Describe the morphology of the erythrocytes.
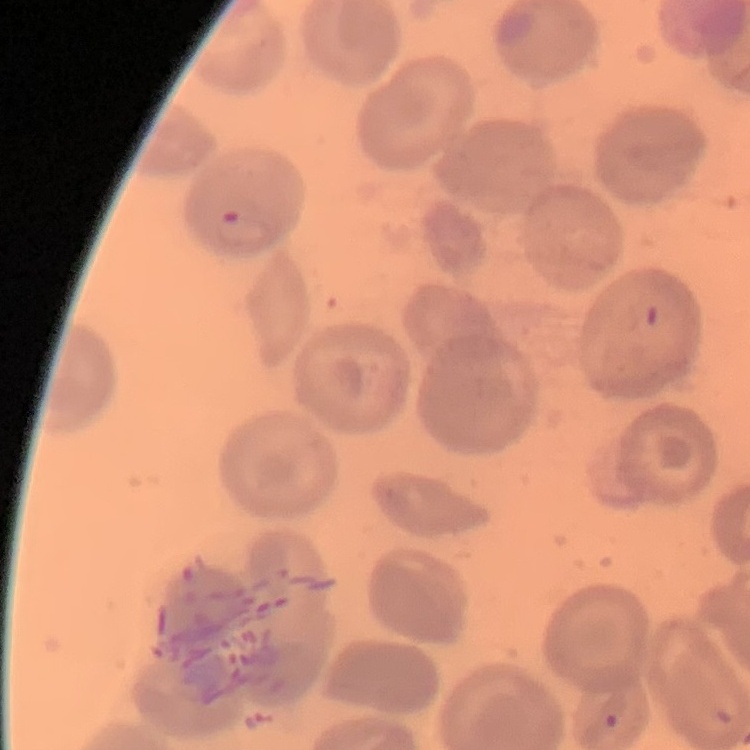

No rouleaux formation.

Summary:
  - Stain: Field's or Giemsa
  - Preparation: thin blood smear
  - Image type: square crop of a larger photomicrograph